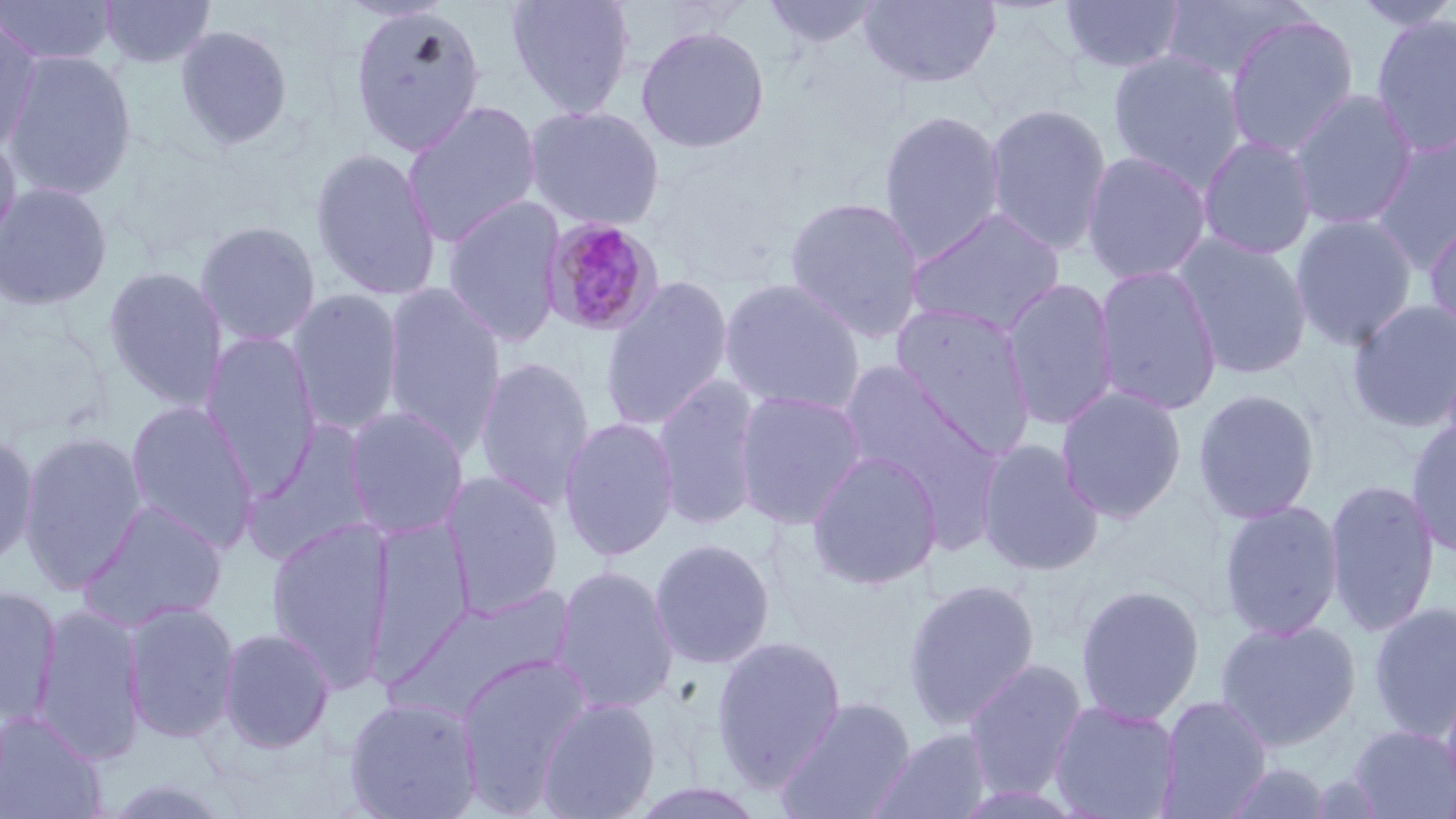

slide-level diagnosis = Plasmodium malariae
modality = light microscopy
field of view = one of a larger specimen
Plasmodium malariae-infected red blood cell locations = approximate bounding boxes as [x1, y1, x2, y2] in pixels: [541, 217, 664, 337]
magnification = 1000x
stain = May-Grünwald-Giemsa
image size = 1456×819 pixels
preparation = thin blood film
uninfected red blood cell locations = approximate bounding boxes as [x1, y1, x2, y2] in pixels: [0, 0, 117, 66], [98, 0, 216, 69], [505, 0, 636, 119], [759, 0, 885, 53], [859, 0, 1002, 89], [1160, 0, 1314, 82], [1349, 0, 1456, 33], [1057, 1, 1188, 76], [348, 3, 488, 156], [1369, 12, 1456, 158], [1222, 13, 1360, 160], [0, 16, 44, 154], [175, 24, 293, 151], [634, 24, 771, 154], [1107, 49, 1247, 191], [2, 50, 138, 202], [1287, 88, 1420, 231], [401, 100, 544, 247], [983, 102, 1114, 256], [524, 104, 666, 231], [877, 109, 1007, 264], [1368, 131, 1456, 273], [0, 133, 23, 259], [1196, 134, 1318, 260], [309, 147, 442, 301], [1080, 150, 1212, 286], [0, 181, 114, 311], [441, 194, 567, 348], [783, 195, 927, 344], [905, 206, 1068, 338], [1290, 214, 1418, 352], [1423, 215, 1456, 340], [194, 220, 322, 347], [1173, 233, 1313, 380], [1092, 263, 1223, 417], [102, 265, 229, 412], [598, 275, 735, 432], [718, 277, 866, 416], [1001, 277, 1120, 430], [380, 283, 507, 455], [287, 288, 406, 436], [1347, 298, 1456, 434], [888, 301, 1037, 459], [200, 330, 323, 496], [473, 355, 596, 511], [834, 359, 995, 501], [652, 374, 765, 532], [1055, 385, 1188, 523], [1192, 388, 1321, 524], [733, 389, 868, 530], [124, 399, 261, 554], [342, 405, 470, 541], [558, 415, 680, 562], [1405, 418, 1456, 559], [241, 419, 379, 566], [17, 430, 149, 594], [0, 431, 40, 571], [975, 437, 1105, 578], [805, 449, 943, 590], [441, 470, 565, 619], [1323, 478, 1440, 638], [79, 499, 229, 631], [1217, 499, 1345, 641], [368, 516, 475, 678], [265, 518, 393, 690], [648, 537, 776, 669], [550, 564, 680, 715], [902, 578, 1042, 731], [1075, 583, 1205, 724], [398, 584, 580, 718], [0, 586, 63, 725], [121, 599, 240, 744], [1366, 600, 1456, 743], [31, 603, 147, 765], [1215, 618, 1361, 752], [217, 627, 336, 755], [710, 634, 846, 789], [455, 652, 593, 815], [963, 658, 1089, 802], [1440, 674, 1456, 808], [343, 695, 483, 819], [1158, 695, 1272, 817], [775, 696, 916, 819], [536, 697, 662, 819], [1048, 699, 1181, 818], [0, 709, 107, 819], [1346, 723, 1456, 818], [869, 727, 995, 819], [1217, 762, 1338, 819], [95, 776, 242, 819]